Classify this cell by malaria status.
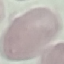

Uninfected.

Summary:
  - Image type: automatically extracted cell patch, resized to 64 × 64 pixels
  - Preparation: thin blood smear
  - Stain: Giemsa
  - Capture: smartphone through the microscope eyepiece